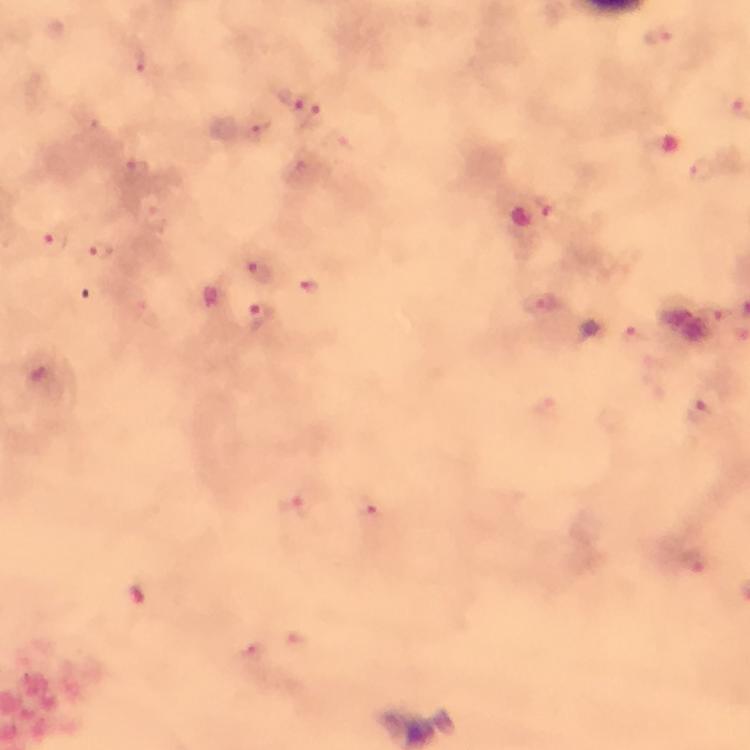
cropped_from: one field of view
malaria_parasite_locations: 'approximate object centers, in pixels from the top-left corner: (x=660, y=38), (x=290, y=100), (x=255, y=130), (x=703, y=169), (x=136, y=171), (x=539, y=209), (x=55, y=242), (x=99, y=252), (x=256, y=271), (x=312, y=289), (x=539, y=304), (x=258, y=320), (x=634, y=339), (x=700, y=414), (x=297, y=503), (x=375, y=514), (x=693, y=560), (x=250, y=651)'
preparation: thick blood film
image_size: 750×750 pixels
context: from a malaria diagnostic workup
immersion_oil: applied
capture: smartphone camera through the microscope
stain: Giemsa
magnification: 100x